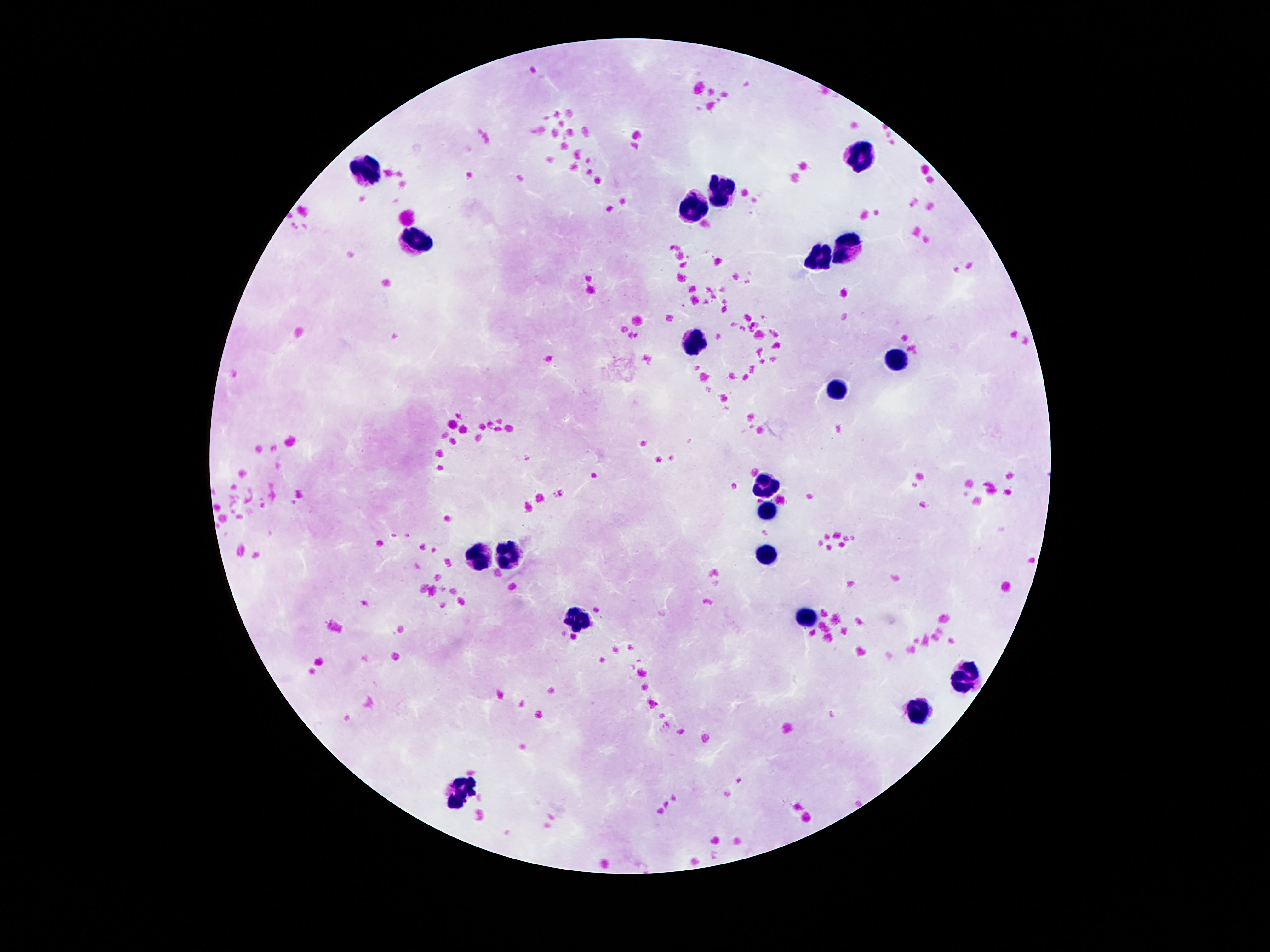

field of view = one from this slide
preparation = thick blood smear
stain = Giemsa
capture = smartphone camera through the microscope eyepiece
leukocyte locations = approximate centers as (x, y) in pixels: (863, 155), (368, 171), (720, 193), (689, 206), (415, 240), (847, 244), (820, 259), (693, 343), (898, 358), (833, 390), (765, 488), (767, 511), (507, 555), (765, 556), (478, 560), (806, 614), (579, 622), (964, 675), (915, 712), (456, 793)
patient malaria status = negative
image size = 1270×952 pixels
magnification = 100x